Classify this cell by malaria status.
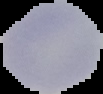

It is uninfected.

Cell region segmented out of the field of view; the surrounding area is masked to black. Image is 103×94 pixels. From a thin blood film.